Assess this cell for malaria.
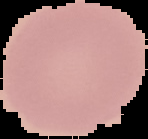

It is uninfected.

The area outside the segmented cell region is set to black. Image is 148×139 pixels. From a thin blood film.